Locate every blood parasite and identify its species.
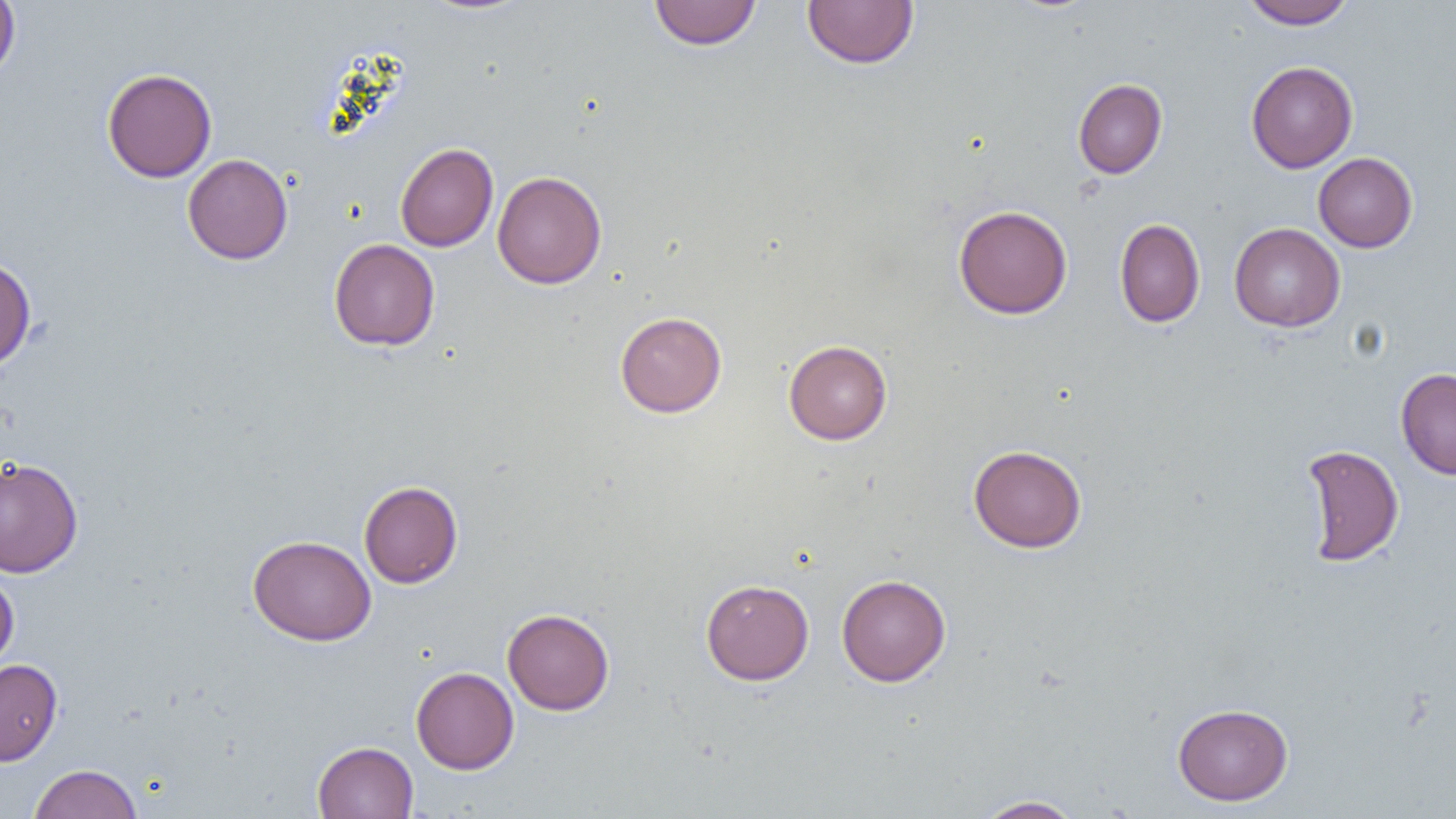

No blood parasites observed.

Approximate bounding boxes as named x1/y1/x2/y2 corners in pixels. Uninfected red blood cell locations: (x1=0, y1=0, x2=20, y2=83), (x1=649, y1=0, x2=761, y2=50), (x1=802, y1=0, x2=919, y2=69), (x1=1240, y1=0, x2=1356, y2=29), (x1=1246, y1=61, x2=1358, y2=173), (x1=102, y1=67, x2=217, y2=182), (x1=1073, y1=78, x2=1167, y2=179), (x1=395, y1=142, x2=498, y2=252), (x1=1313, y1=152, x2=1417, y2=252), (x1=182, y1=153, x2=293, y2=265), (x1=492, y1=171, x2=607, y2=289), (x1=953, y1=205, x2=1072, y2=319), (x1=1114, y1=218, x2=1205, y2=327), (x1=1229, y1=222, x2=1346, y2=332), (x1=329, y1=238, x2=440, y2=351), (x1=0, y1=255, x2=36, y2=372), (x1=615, y1=311, x2=727, y2=418), (x1=783, y1=339, x2=892, y2=444), (x1=1395, y1=367, x2=1456, y2=480), (x1=968, y1=444, x2=1087, y2=553), (x1=1299, y1=444, x2=1404, y2=567), (x1=0, y1=455, x2=84, y2=578), (x1=359, y1=480, x2=463, y2=588), (x1=247, y1=535, x2=376, y2=646), (x1=0, y1=572, x2=19, y2=671), (x1=836, y1=574, x2=951, y2=686), (x1=701, y1=578, x2=814, y2=685), (x1=502, y1=608, x2=615, y2=715), (x1=0, y1=658, x2=62, y2=766), (x1=411, y1=666, x2=519, y2=774), (x1=1172, y1=703, x2=1293, y2=806), (x1=312, y1=741, x2=419, y2=818), (x1=28, y1=763, x2=142, y2=819), (x1=974, y1=795, x2=1084, y2=818). Slide-level diagnosis: no evidence of blood parasites. Thin blood smear. One field of a larger specimen. Light microscopy. Captured at 1000x magnification. Image is 1456×819 pixels.